Locate every leukocyte (white blood cell).
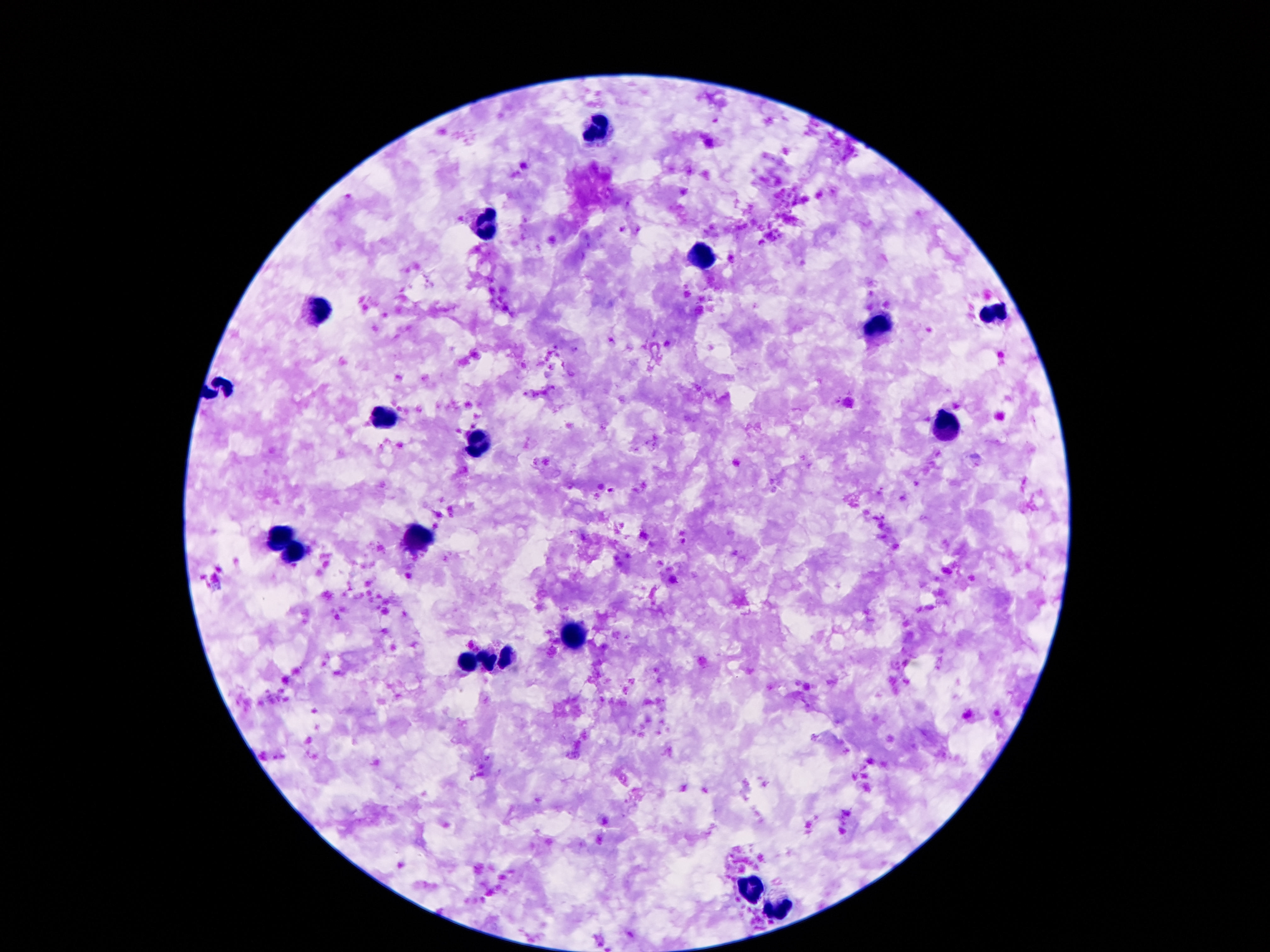

Approximate object centers, in pixels from the top-left corner.
Leukocytes: (x=602, y=129), (x=490, y=225), (x=703, y=258), (x=315, y=313), (x=992, y=315), (x=878, y=326), (x=384, y=418), (x=944, y=429), (x=477, y=446), (x=421, y=538), (x=281, y=541), (x=296, y=552), (x=574, y=634), (x=468, y=661), (x=498, y=661), (x=754, y=884), (x=778, y=909).

capture = smartphone camera through the microscope eyepiece
magnification = 100x
field of view = one from this slide
preparation = thick blood smear
image size = 1270×952 pixels
stain = Giemsa
patient malaria status = not infected